Report the malaria status of this cell.
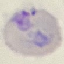
It is parasitized.

Summary:
  - Capture: smartphone camera at the microscope eyepiece
  - Stain: Giemsa
  - Image type: automatically extracted cell patch, resized to 64 × 64 pixels
  - Preparation: thin blood smear